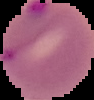 From a thin blood smear. Image is 94×100 pixels. Malaria status: parasitized. Segmented cell region on a black background.